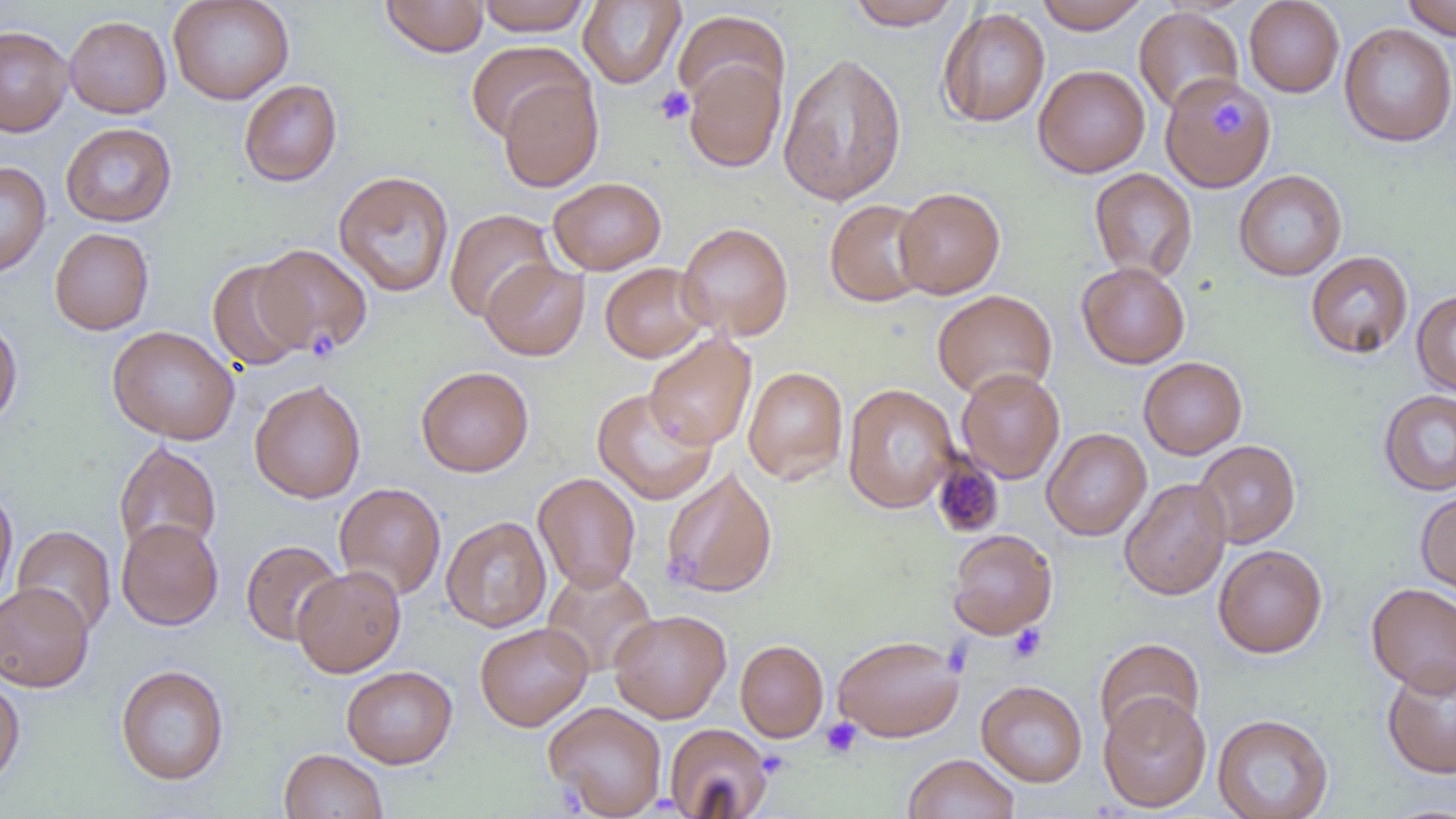

Approximate bounding boxes as (x1,y1)-(x2,y2) corner pairs in pixels. Uninfected red blood cell locations: (167,0)-(295,105), (381,0)-(489,57), (476,0)-(593,35), (1033,0)-(1150,33), (1244,0)-(1345,97), (1401,0)-(1456,40), (578,1)-(686,89), (846,1)-(964,30), (1133,6)-(1244,114), (937,7)-(1050,128), (672,10)-(790,115), (64,15)-(171,118), (1339,23)-(1456,147), (0,25)-(73,136), (465,41)-(591,144), (777,52)-(907,206), (683,58)-(786,173), (1033,64)-(1150,178), (497,75)-(604,192), (1159,75)-(1275,193), (239,79)-(342,186), (61,122)-(177,227), (0,161)-(51,277), (1089,168)-(1198,283), (333,170)-(454,297), (1234,170)-(1347,281), (548,177)-(666,275), (894,187)-(1005,299), (824,199)-(933,307), (445,209)-(557,322), (677,222)-(794,341), (50,227)-(154,335), (255,244)-(373,358), (1305,251)-(1413,359), (480,258)-(590,361), (206,259)-(309,371), (600,262)-(710,363), (1077,262)-(1190,369), (932,289)-(1058,400), (1411,290)-(1456,396), (0,314)-(23,429), (107,325)-(240,445), (643,331)-(757,450), (1138,357)-(1247,459), (416,366)-(534,477), (743,366)-(849,484), (956,368)-(1065,484), (249,379)-(366,504), (842,383)-(959,513), (592,388)-(718,505), (1378,390)-(1456,496), (1041,428)-(1152,541), (1192,439)-(1301,548), (113,441)-(222,558), (660,466)-(779,599), (533,473)-(641,592), (1118,477)-(1232,600), (334,482)-(447,600), (0,486)-(17,608), (1416,490)-(1456,596), (441,516)-(552,633), (116,518)-(224,630), (12,524)-(116,637), (947,529)-(1058,639), (241,540)-(345,645), (1213,544)-(1327,658), (292,566)-(406,677), (541,566)-(658,678), (0,582)-(94,692), (1366,583)-(1456,695), (609,609)-(731,723), (474,621)-(593,731), (832,634)-(964,742), (1094,637)-(1205,742), (735,639)-(829,742), (1381,662)-(1456,779), (115,664)-(229,785), (341,665)-(458,768), (0,673)-(25,788), (976,680)-(1088,787), (1098,692)-(1212,813), (544,701)-(667,817), (1212,713)-(1333,819), (664,723)-(773,819), (279,748)-(388,819), (904,753)-(1020,819). Platelet locations: (654,85)-(695,125), (1212,104)-(1245,139), (307,326)-(339,353), (931,457)-(1004,537), (666,558)-(711,588), (1008,624)-(1047,662), (821,717)-(862,758), (757,750)-(791,780), (559,781)-(587,812). Slide-level diagnosis: negative for blood parasites. 1000x magnification. One field of a larger specimen. Thin blood film. Image is 1456×819 pixels. Optical microscopy.